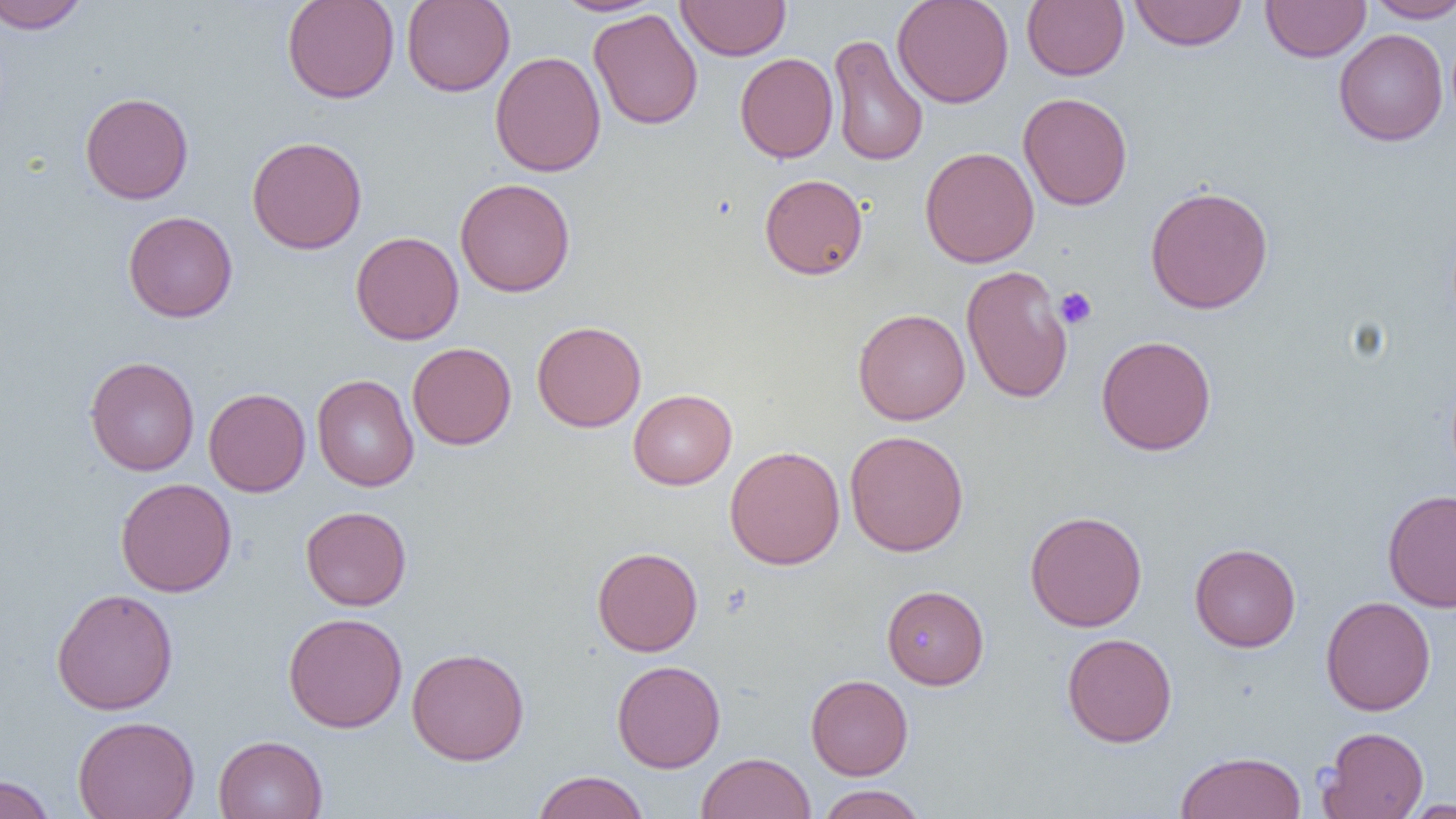
slide-level diagnosis = no evidence of blood parasites
preparation = thin blood smear
modality = light microscopy
uninfected red blood cell locations = approximate bounding boxes as named x1/y1/x2/y2 corners in pixels: (x1=0, y1=0, x2=91, y2=33), (x1=282, y1=0, x2=400, y2=103), (x1=401, y1=0, x2=515, y2=97), (x1=551, y1=0, x2=664, y2=16), (x1=676, y1=0, x2=791, y2=61), (x1=891, y1=0, x2=1014, y2=108), (x1=1129, y1=0, x2=1248, y2=51), (x1=1364, y1=0, x2=1456, y2=22), (x1=1022, y1=1, x2=1129, y2=80), (x1=1261, y1=1, x2=1371, y2=62), (x1=588, y1=8, x2=703, y2=130), (x1=1334, y1=29, x2=1448, y2=146), (x1=827, y1=33, x2=928, y2=167), (x1=490, y1=51, x2=606, y2=177), (x1=735, y1=52, x2=838, y2=163), (x1=80, y1=91, x2=194, y2=204), (x1=1018, y1=92, x2=1133, y2=211), (x1=246, y1=136, x2=367, y2=254), (x1=920, y1=147, x2=1040, y2=268), (x1=759, y1=174, x2=868, y2=279), (x1=455, y1=178, x2=575, y2=297), (x1=1145, y1=185, x2=1274, y2=314), (x1=123, y1=211, x2=238, y2=323), (x1=350, y1=231, x2=464, y2=344), (x1=960, y1=264, x2=1073, y2=405), (x1=853, y1=308, x2=970, y2=425), (x1=532, y1=321, x2=647, y2=432), (x1=1096, y1=334, x2=1217, y2=455), (x1=406, y1=342, x2=517, y2=450), (x1=84, y1=356, x2=199, y2=476), (x1=311, y1=374, x2=419, y2=491), (x1=203, y1=387, x2=311, y2=497), (x1=628, y1=388, x2=737, y2=489), (x1=844, y1=430, x2=969, y2=556), (x1=724, y1=445, x2=845, y2=570), (x1=115, y1=478, x2=237, y2=597), (x1=1383, y1=489, x2=1456, y2=613), (x1=300, y1=506, x2=412, y2=610), (x1=1024, y1=511, x2=1148, y2=632), (x1=1189, y1=543, x2=1301, y2=652), (x1=592, y1=547, x2=703, y2=656), (x1=882, y1=585, x2=989, y2=689), (x1=51, y1=588, x2=179, y2=715), (x1=1321, y1=596, x2=1436, y2=716), (x1=283, y1=612, x2=408, y2=733), (x1=1061, y1=633, x2=1177, y2=747), (x1=406, y1=647, x2=530, y2=765), (x1=612, y1=660, x2=726, y2=772), (x1=805, y1=674, x2=914, y2=780), (x1=72, y1=715, x2=200, y2=819), (x1=1317, y1=726, x2=1429, y2=819), (x1=213, y1=734, x2=327, y2=819), (x1=1175, y1=751, x2=1306, y2=819), (x1=697, y1=752, x2=815, y2=819), (x1=531, y1=770, x2=649, y2=819), (x1=0, y1=775, x2=56, y2=819), (x1=816, y1=784, x2=928, y2=819), (x1=1398, y1=798, x2=1456, y2=818)
platelet locations = approximate bounding boxes as named x1/y1/x2/y2 corners in pixels: (x1=1054, y1=287, x2=1097, y2=329)
magnification = 1000x
field of view = single
image size = 1456×819 pixels